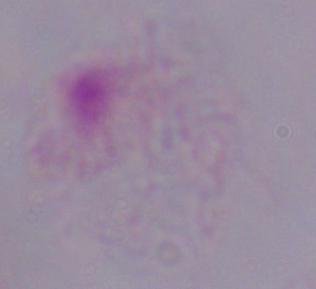

Summary:
  - Magnification: 1000x
  - Identification: trichomonad
  - Modality: micrograph